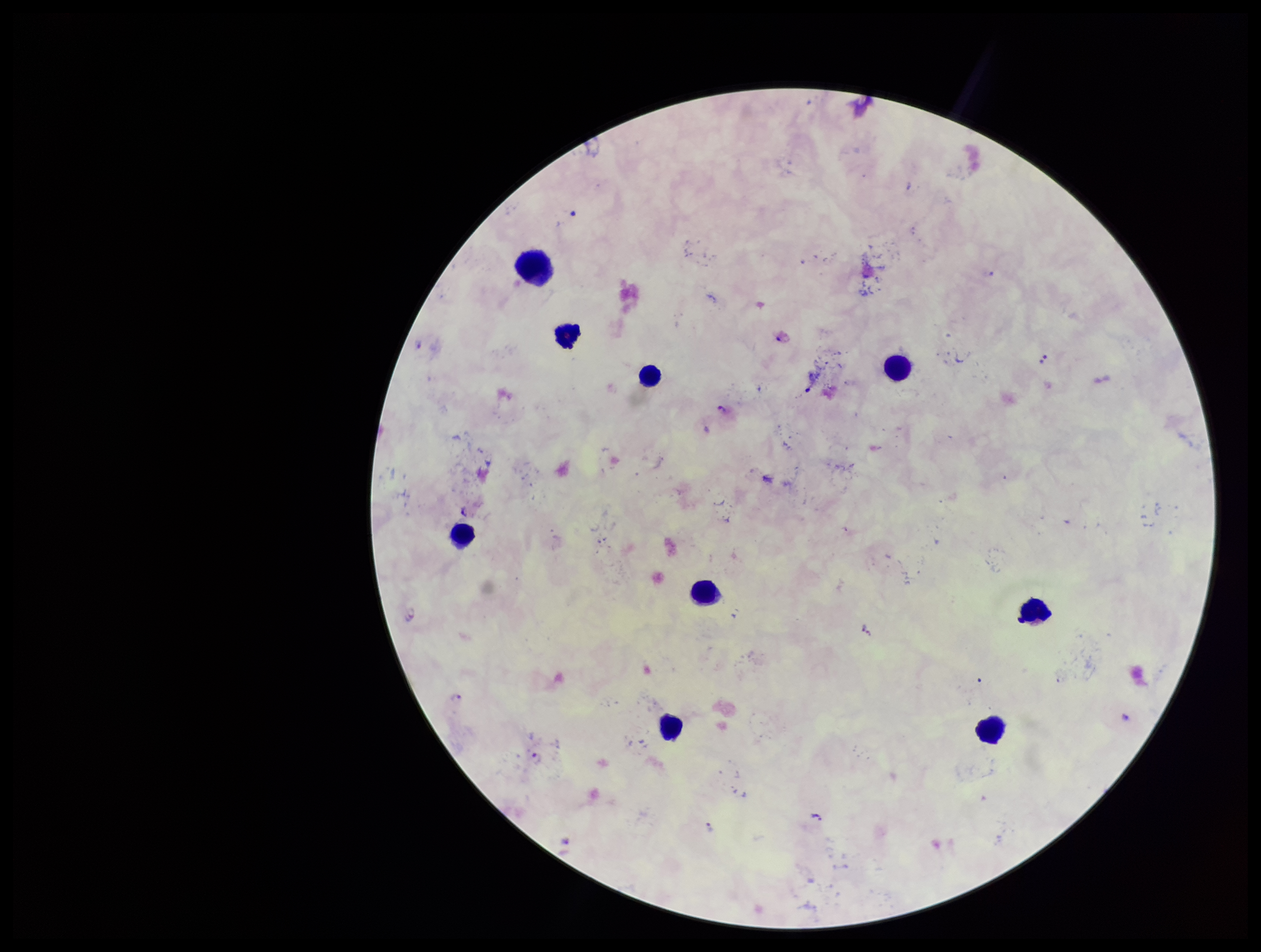

Summary:
  - Species reported for this patient: Plasmodium falciparum
  - Stain: Giemsa
  - Parasite count: 6
  - Preparation: thick
  - Capture: smartphone photograph through the microscope eyepiece
  - Image size: 1261×952 pixels
  - Patient malaria status: positive
  - Plasmodium parasites: seen
  - Leukocyte count: 9
  - Field of view: single